Describe the morphology of the red blood cells.
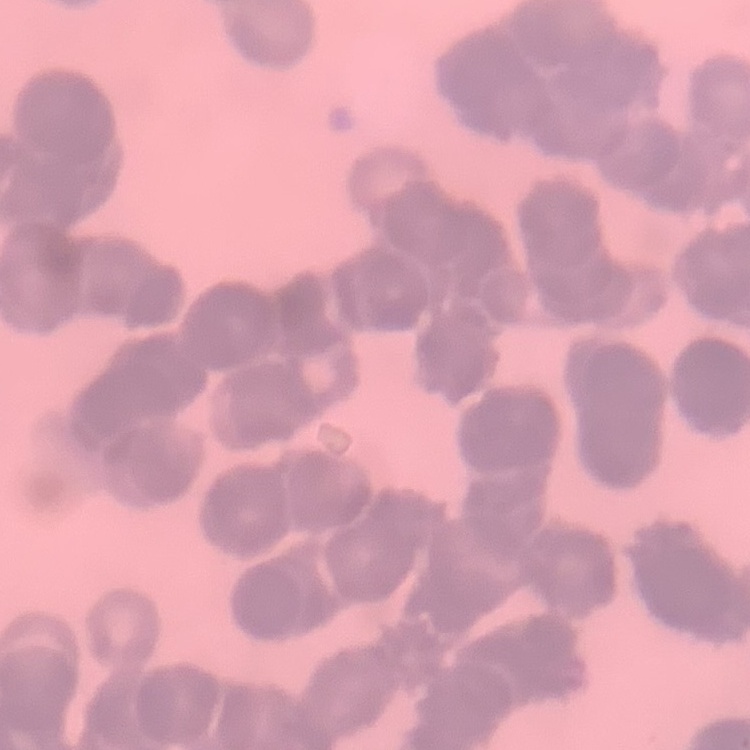

They show rouleaux formation.

Stained with either Field's or Giemsa. Thin blood film. Square crop of a larger photomicrograph.